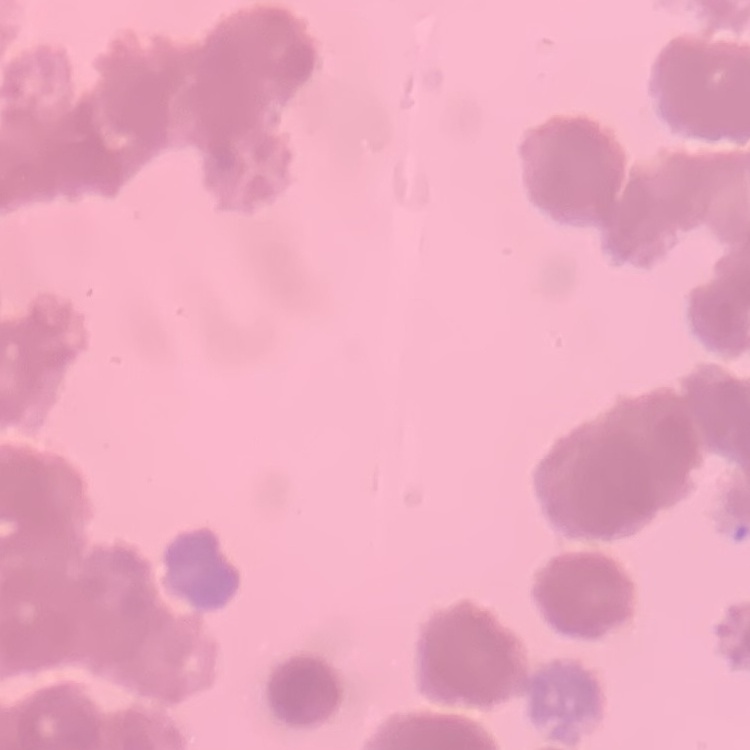
Summary:
  - Erythrocyte morphology: rouleaux formation
  - Preparation: thin blood smear
  - Stain: Field's or Giemsa
  - Image type: one tile cut from a larger photomicrograph